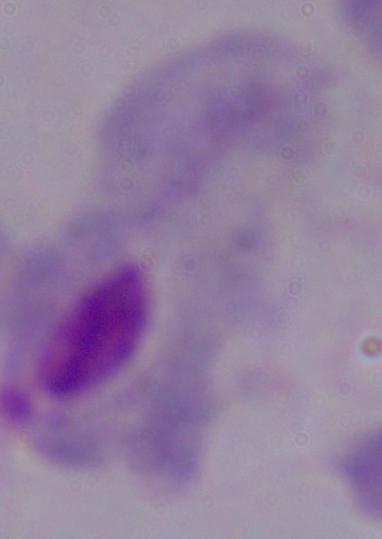
magnification = 1000x
modality = micrograph
identification = trichomonad